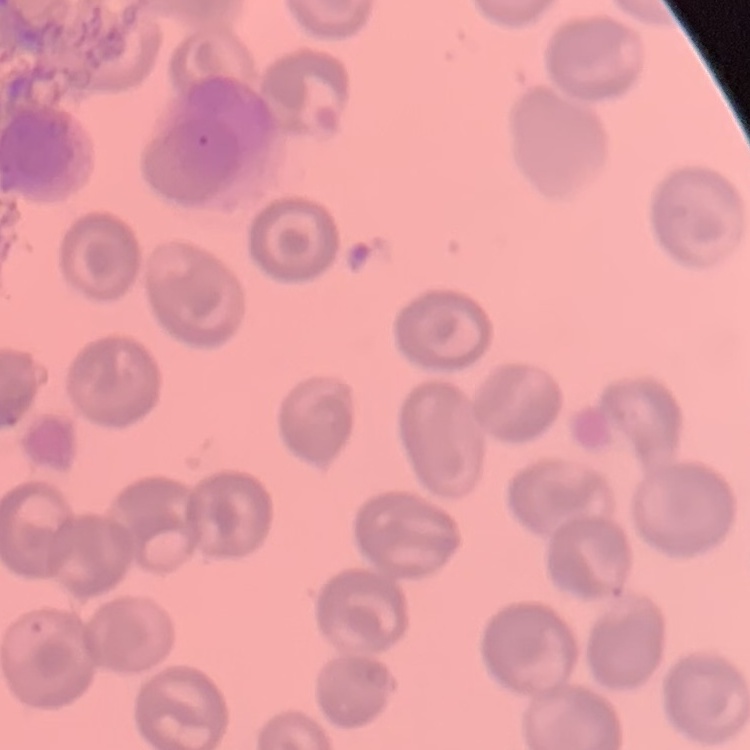
Summary:
  - Red blood cell morphology: no rouleaux formation
  - Preparation: thin peripheral smear
  - Image type: square crop of a larger photomicrograph
  - Stain: Field's or Giemsa